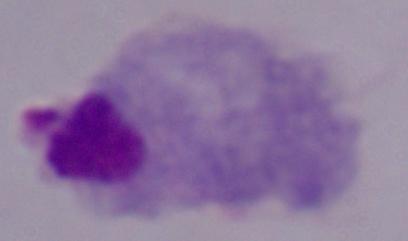

{
  "identification": "trichomonad",
  "modality": "micrograph",
  "magnification": "1000x"
}